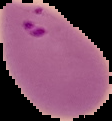

result: Plasmodium parasites identified
preparation: thin blood smear
image_type: segmented cell region with the area outside set to black
image_size: 112×121 pixels